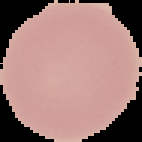

Cell region segmented out of the field of view; the surrounding area is masked to black. Image is 142×142 pixels. Malaria status: uninfected. From a thin blood film.